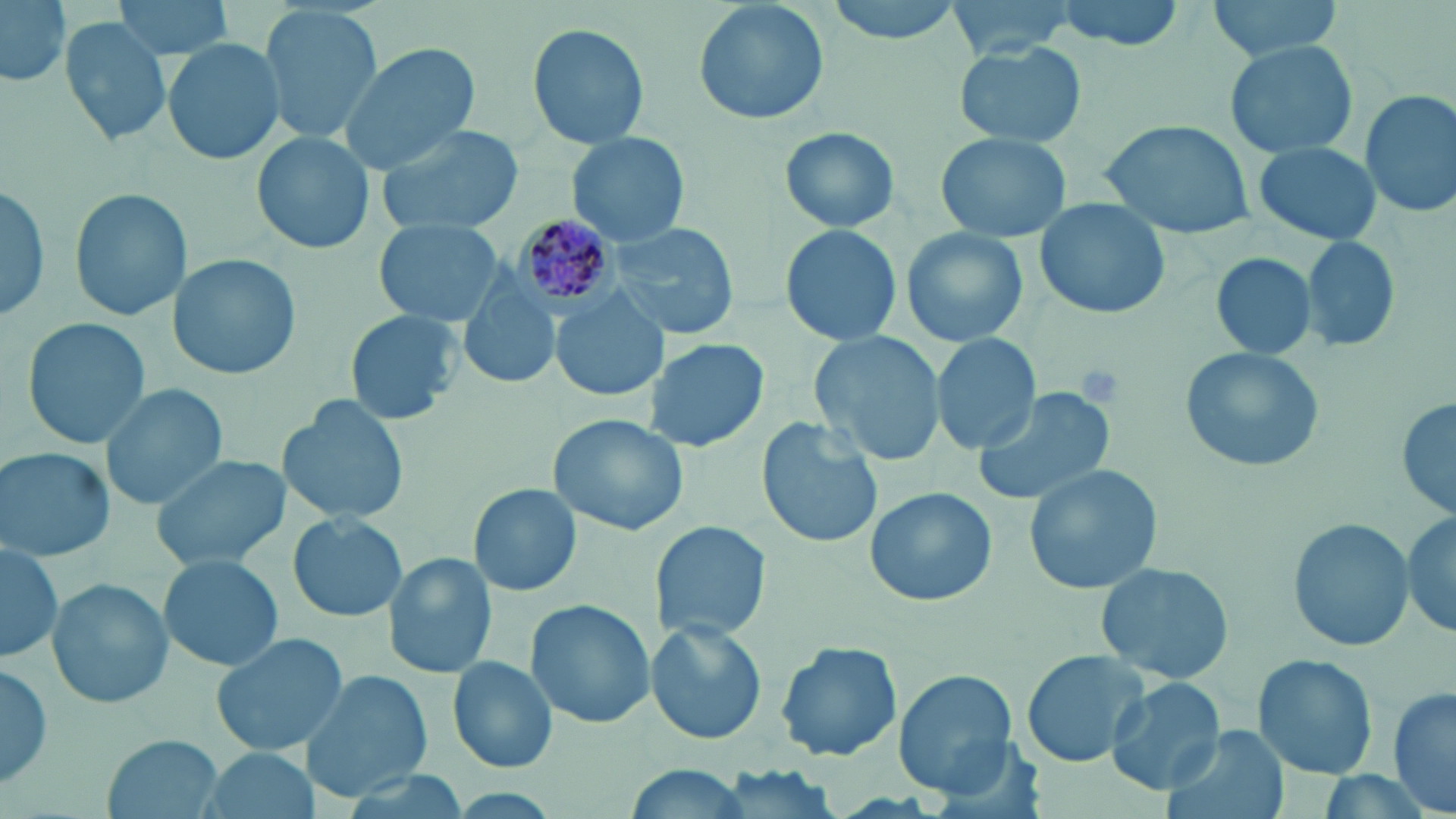
Approximate bounding boxes as (x1, y1, x2, y2) in pixels. Platelet locations: (1075, 363, 1126, 407). Uninfected red blood cell locations: (1, 0, 71, 87), (113, 0, 235, 59), (693, 0, 829, 126), (820, 0, 968, 42), (937, 0, 1090, 62), (1051, 0, 1188, 50), (1206, 0, 1348, 60), (258, 3, 383, 146), (60, 15, 173, 145), (528, 21, 650, 150), (163, 38, 287, 168), (953, 39, 1087, 148), (1225, 39, 1359, 160), (340, 41, 481, 173), (1358, 89, 1456, 218), (1100, 118, 1258, 240), (372, 124, 523, 234), (778, 126, 900, 235), (253, 130, 375, 254), (567, 133, 693, 249), (937, 134, 1071, 242), (1251, 141, 1383, 246), (0, 183, 52, 322), (69, 187, 189, 323), (1031, 198, 1172, 321), (611, 218, 739, 343), (373, 219, 506, 329), (779, 223, 903, 348), (902, 227, 1029, 347), (1301, 234, 1402, 354), (169, 252, 300, 382), (1208, 252, 1318, 360), (459, 273, 562, 391), (553, 292, 666, 402), (344, 309, 462, 426), (21, 315, 151, 450), (810, 332, 946, 468), (931, 333, 1043, 455), (645, 337, 768, 453), (1178, 346, 1324, 473), (102, 382, 227, 511), (973, 385, 1118, 507), (1395, 391, 1455, 526), (279, 394, 409, 526), (549, 414, 690, 536), (757, 416, 882, 548), (1, 447, 115, 563), (150, 454, 289, 573), (1024, 461, 1165, 596), (468, 483, 582, 597), (865, 488, 998, 605), (1404, 508, 1453, 641), (288, 511, 406, 623), (1288, 518, 1414, 654), (649, 520, 771, 643), (0, 540, 63, 663), (158, 553, 284, 673), (385, 553, 499, 680), (1096, 561, 1234, 685), (46, 577, 173, 710), (524, 600, 656, 729), (645, 622, 767, 745), (209, 631, 354, 758), (774, 641, 903, 763), (1020, 649, 1152, 769), (1251, 653, 1380, 778), (446, 655, 558, 773), (0, 663, 55, 791), (300, 670, 435, 800), (893, 670, 1019, 797), (1104, 676, 1228, 796), (1388, 685, 1456, 815), (1162, 728, 1288, 819), (102, 732, 224, 817), (194, 748, 322, 819), (613, 764, 756, 819). Plasmodium malariae-infected red blood cell locations: (512, 214, 616, 309). Slide-level diagnosis: Plasmodium malariae. One field of a larger specimen. May-Grünwald-Giemsa stain. Image is 1456×819 pixels. Captured at 1000x magnification. Optical microscopy. Thin blood smear.